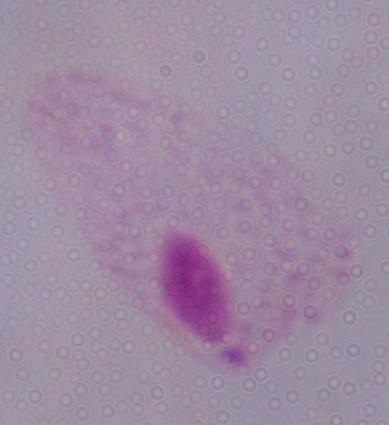
Summary:
  - Magnification: 1000x
  - Identification: trichomonad
  - Modality: photomicrograph